Assess this cell for malaria.
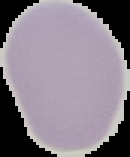
It is uninfected.

Summary:
  - Image type: segmented cell region with the area outside set to black
  - Preparation: thin blood film
  - Image size: 130×157 pixels